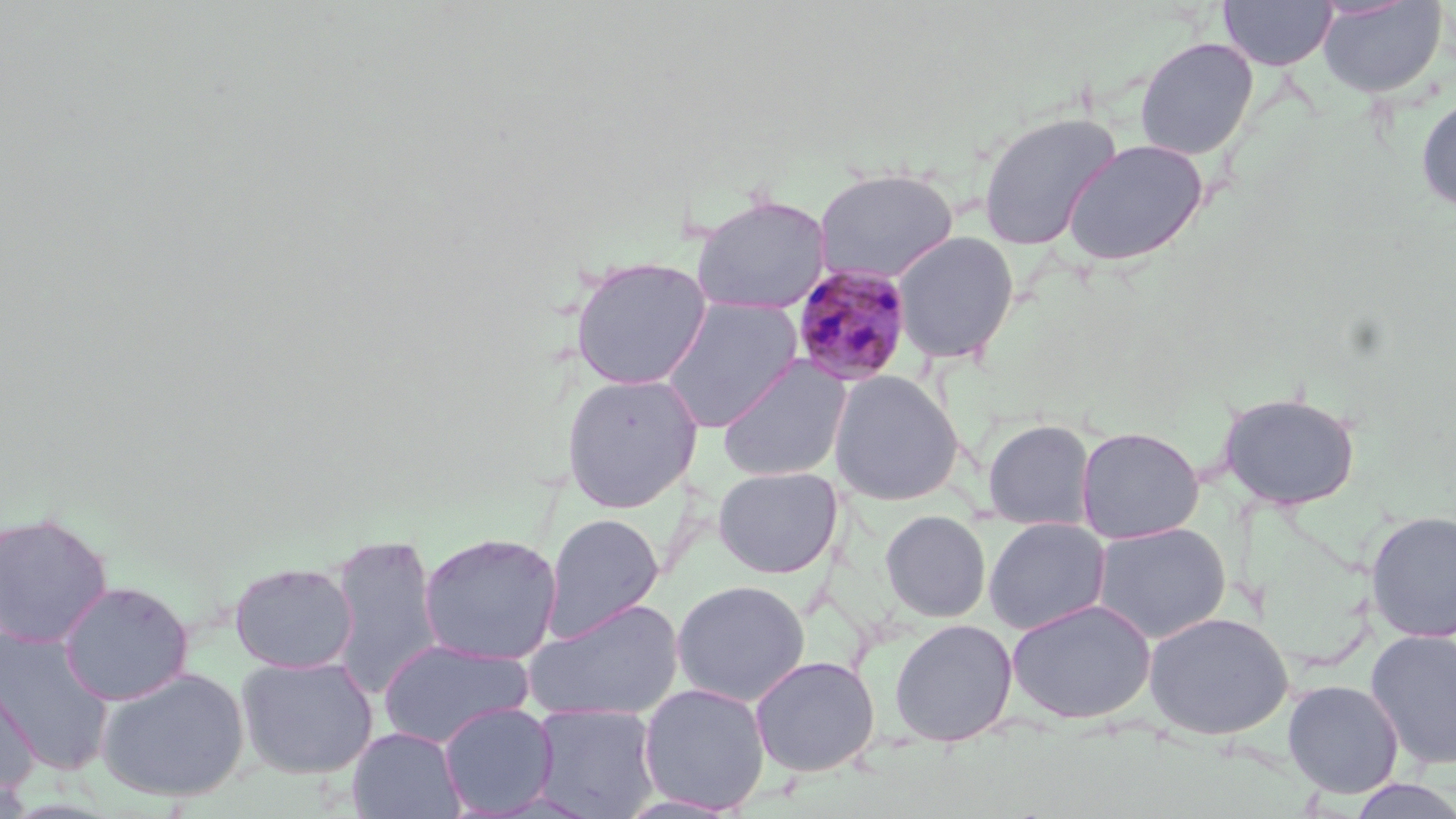
Summary:
  - Coordinate format: approximate bounding boxes as [x1, y1, x2, y2] in pixels
  - Plasmodium malariae-infected red blood cell locations: [789, 263, 914, 386]
  - Uninfected red blood cell locations: [1218, 0, 1337, 71], [1317, 0, 1447, 98], [1134, 36, 1259, 160], [1415, 93, 1456, 213], [977, 110, 1123, 251], [1062, 138, 1208, 267], [813, 166, 959, 284], [690, 193, 832, 315], [892, 230, 1020, 365], [569, 255, 713, 390], [658, 296, 803, 432], [716, 356, 852, 482], [828, 371, 965, 506], [560, 372, 703, 513], [1220, 390, 1361, 509], [982, 418, 1097, 530], [1076, 426, 1204, 543], [713, 466, 843, 579], [880, 509, 991, 622], [1364, 510, 1456, 642], [0, 511, 113, 647], [542, 512, 664, 641], [983, 516, 1111, 634], [1091, 522, 1231, 643], [328, 532, 444, 700], [418, 532, 563, 666], [229, 560, 358, 673], [671, 579, 812, 706], [57, 580, 194, 705], [525, 598, 685, 722], [1007, 598, 1155, 724], [1143, 611, 1294, 740], [889, 618, 1018, 746], [0, 628, 115, 774], [1365, 629, 1456, 770], [378, 637, 535, 748], [236, 655, 378, 779], [749, 655, 881, 777], [95, 666, 251, 803], [0, 668, 39, 794], [1281, 679, 1404, 799], [638, 682, 771, 814], [438, 702, 558, 816], [530, 702, 662, 819], [348, 727, 466, 819], [1345, 777, 1456, 819]
  - Slide-level diagnosis: Plasmodium malariae
  - Image size: 1456×819 pixels
  - Preparation: thin blood film
  - Modality: optical microscopy
  - Field of view: single
  - Magnification: 1000x
  - Stain: May-Grünwald-Giemsa